State which parasite is depicted.
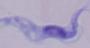
A trypanosome.

modality = photomicrograph
magnification = 1000x